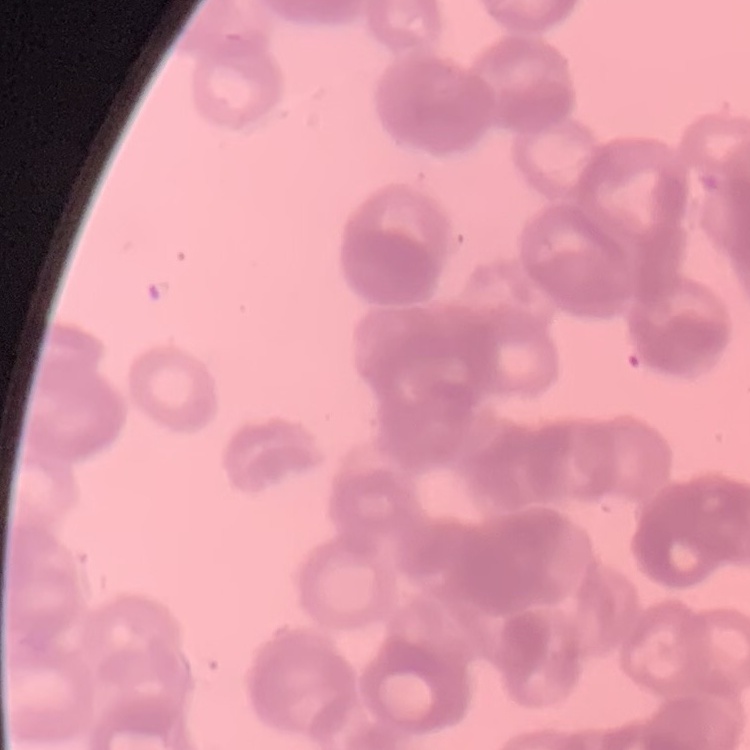

The red blood cells show rouleaux formation. Thin blood film. Square crop of a larger photomicrograph. Stained with either Field's or Giemsa.